Report the malaria status of this cell.
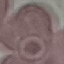
Uninfected.

Giemsa stain. Photographed with a smartphone camera at the microscope eyepiece. Cell patch, automatically extracted from a larger field of view and resized to 64 × 64 pixels. Thin blood smear.